Identify the parasite.
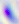
Toxoplasma gondii.

{
  "magnification": "400x",
  "modality": "micrograph"
}